Locate every blood parasite and identify its species.
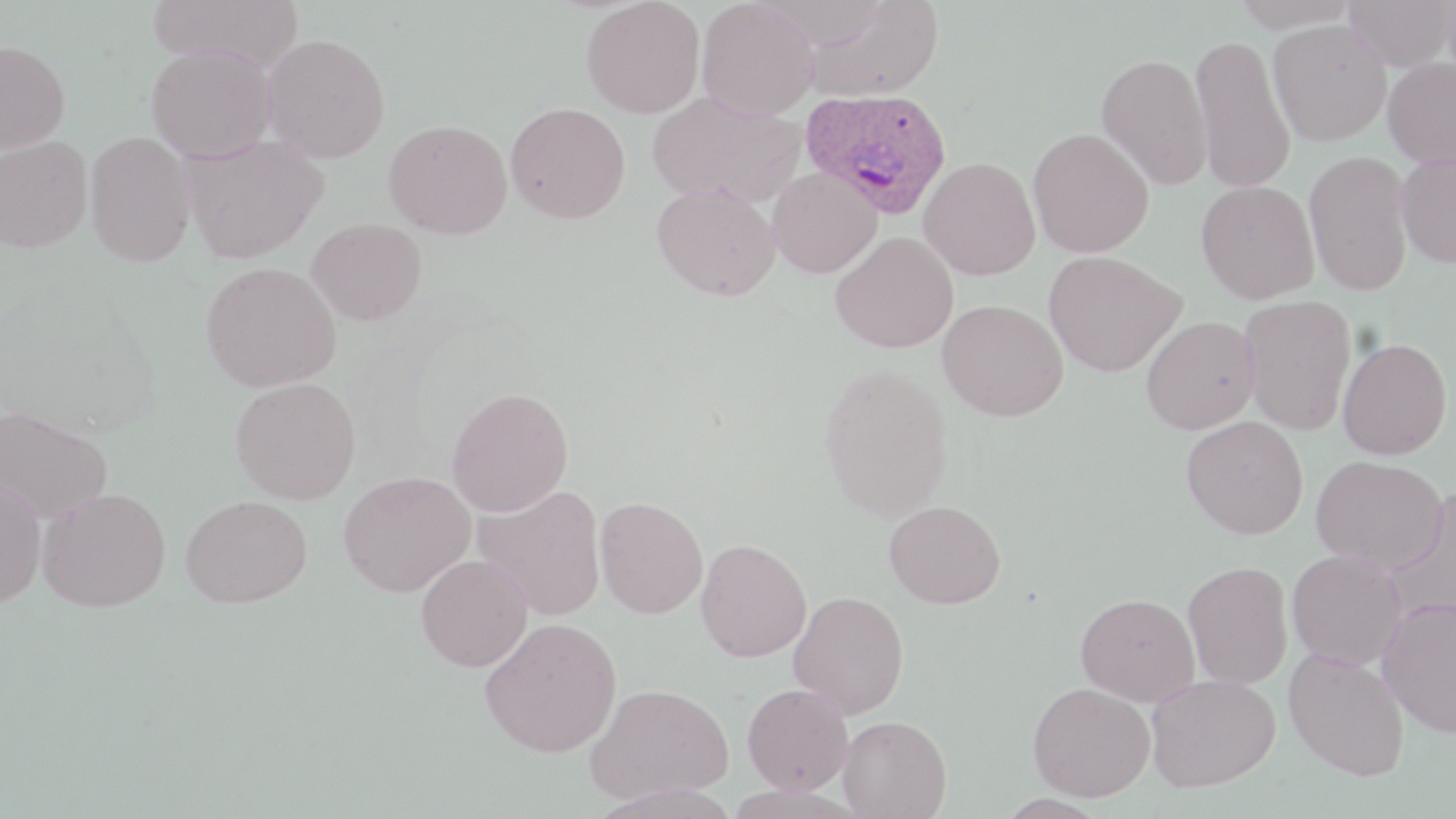

Approximate bounding boxes as [x1, y1, x2, y2] in pixels.
Plasmodium ovale-infected red blood cells: [800, 87, 953, 220].
No Plasmodium falciparum, Plasmodium malariae, Plasmodium vivax, Babesia divergens, or Trypanosoma brucei observed.

slide-level diagnosis = Plasmodium ovale
field of view = single
preparation = thin blood film
magnification = 1000x
modality = light microscopy
image size = 1456×819 pixels
uninfected red blood cell locations = approximate bounding boxes as [x1, y1, x2, y2] in pixels: [147, 0, 302, 69], [580, 0, 706, 118], [696, 0, 819, 121], [1231, 0, 1362, 30], [1342, 0, 1454, 72], [1441, 0, 1456, 90], [802, 1, 944, 102], [1268, 19, 1392, 146], [263, 33, 391, 163], [1189, 33, 1295, 193], [0, 40, 70, 153], [146, 45, 277, 163], [1096, 53, 1213, 190], [1382, 57, 1456, 168], [647, 91, 806, 209], [505, 101, 631, 223], [384, 119, 512, 240], [1027, 127, 1155, 258], [84, 131, 196, 267], [182, 132, 328, 263], [1, 136, 93, 253], [1302, 150, 1415, 295], [1395, 153, 1456, 269], [918, 156, 1041, 280], [767, 167, 882, 279], [1196, 180, 1319, 304], [651, 181, 781, 301], [306, 218, 427, 326], [830, 232, 958, 353], [1043, 250, 1186, 377], [201, 261, 341, 392], [1239, 295, 1356, 435], [938, 299, 1068, 421], [1140, 315, 1260, 434], [1337, 337, 1452, 460], [818, 363, 954, 521], [231, 377, 361, 505], [446, 386, 574, 517], [0, 404, 113, 524], [1181, 415, 1308, 539], [1311, 455, 1447, 573], [338, 470, 476, 596], [0, 476, 47, 607], [473, 484, 606, 620], [37, 487, 171, 612], [1382, 491, 1456, 626], [182, 494, 313, 607], [595, 496, 708, 619], [883, 499, 1006, 609], [695, 538, 812, 662], [1286, 549, 1408, 670], [415, 554, 533, 672], [1182, 560, 1294, 689], [788, 590, 909, 719], [1076, 593, 1200, 706], [1376, 595, 1456, 738], [480, 616, 622, 757], [1284, 648, 1410, 781], [1146, 674, 1281, 792], [585, 682, 732, 805], [742, 682, 853, 795], [1027, 682, 1155, 802], [838, 715, 952, 818]
stain = May-Grünwald-Giemsa